State which cell type is depicted.
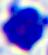

This is a leukocyte.

Photomicrograph. 400x magnification.